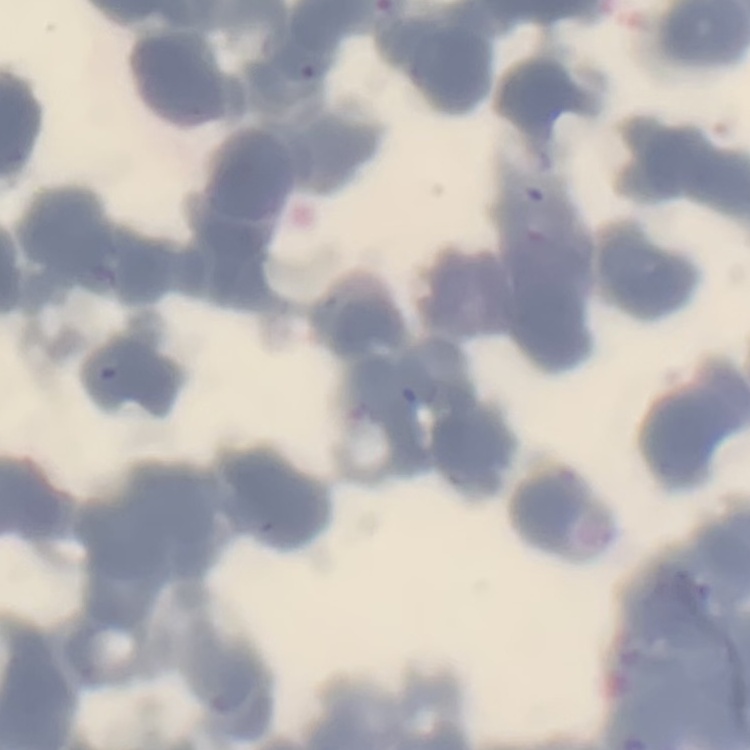

Summary:
  - Red blood cell morphology: rouleaux formation
  - Image type: square crop of a larger photomicrograph
  - Stain: Field's or Giemsa
  - Preparation: thin peripheral smear